Classify this cell by malaria status.
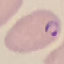

Parasitized.

Giemsa-stained preparation. Cell patch, automatically extracted from a larger field of view and resized to 64 × 64 pixels. Photographed with a smartphone camera at the microscope eyepiece. Thin smear of blood.